Give the position of every leukocyte visible.
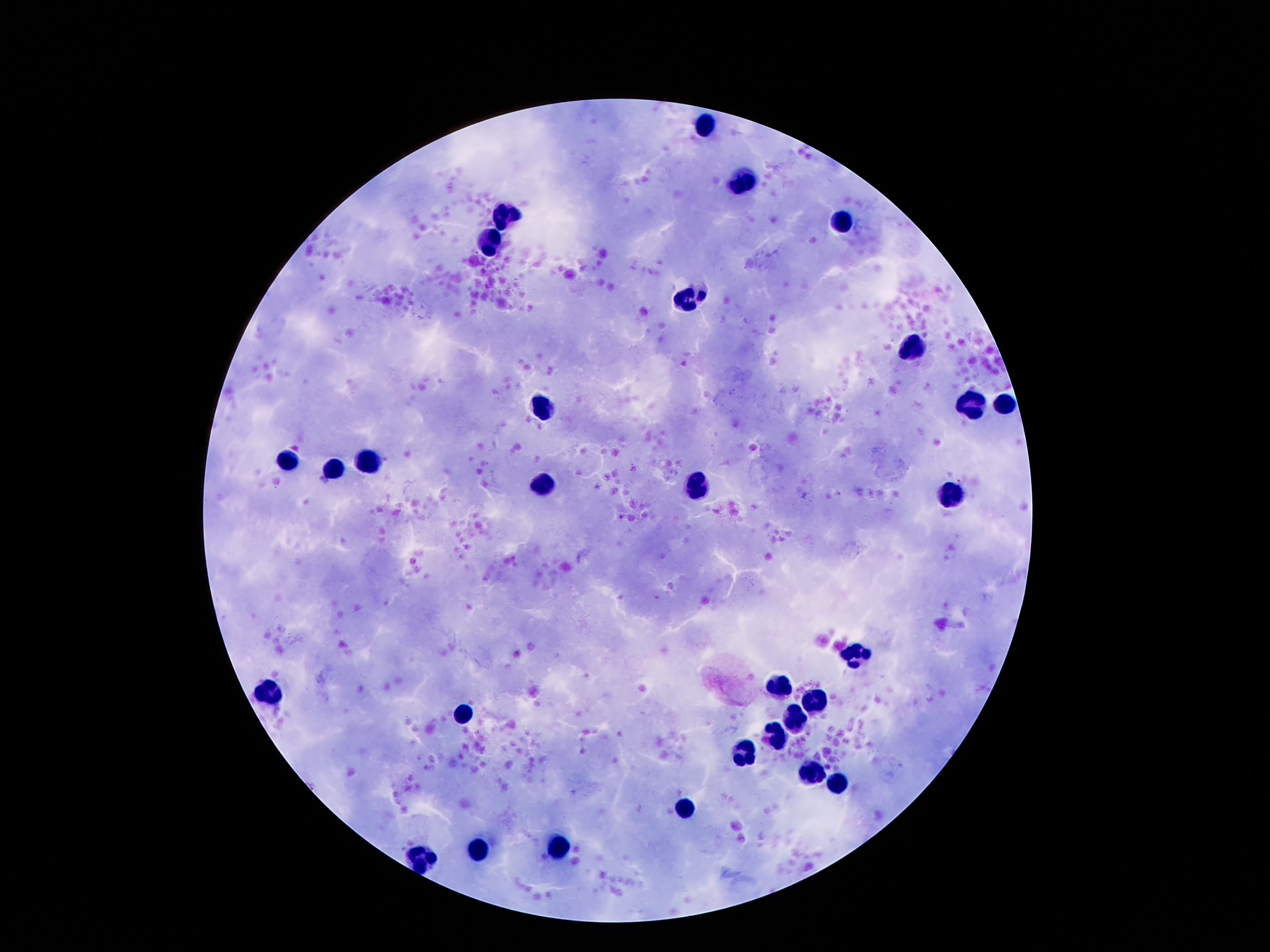
Approximate centers as (x, y) in pixels.
Leukocytes: (705, 124), (742, 182), (508, 215), (842, 220), (490, 239), (688, 295), (912, 347), (973, 403), (1005, 404), (549, 406), (370, 458), (288, 459), (334, 469), (545, 484), (699, 487), (953, 496), (855, 655), (780, 686), (272, 692), (817, 701), (461, 712), (796, 717), (776, 739), (746, 751), (808, 773), (837, 783), (688, 808), (556, 848), (481, 849), (424, 860).

Summary:
  - Image size: 1270×952 pixels
  - Magnification: 100x
  - Preparation: thick blood film
  - Stain: Giemsa
  - Capture: smartphone camera through the microscope eyepiece
  - Patient malaria status: negative
  - Field of view: single